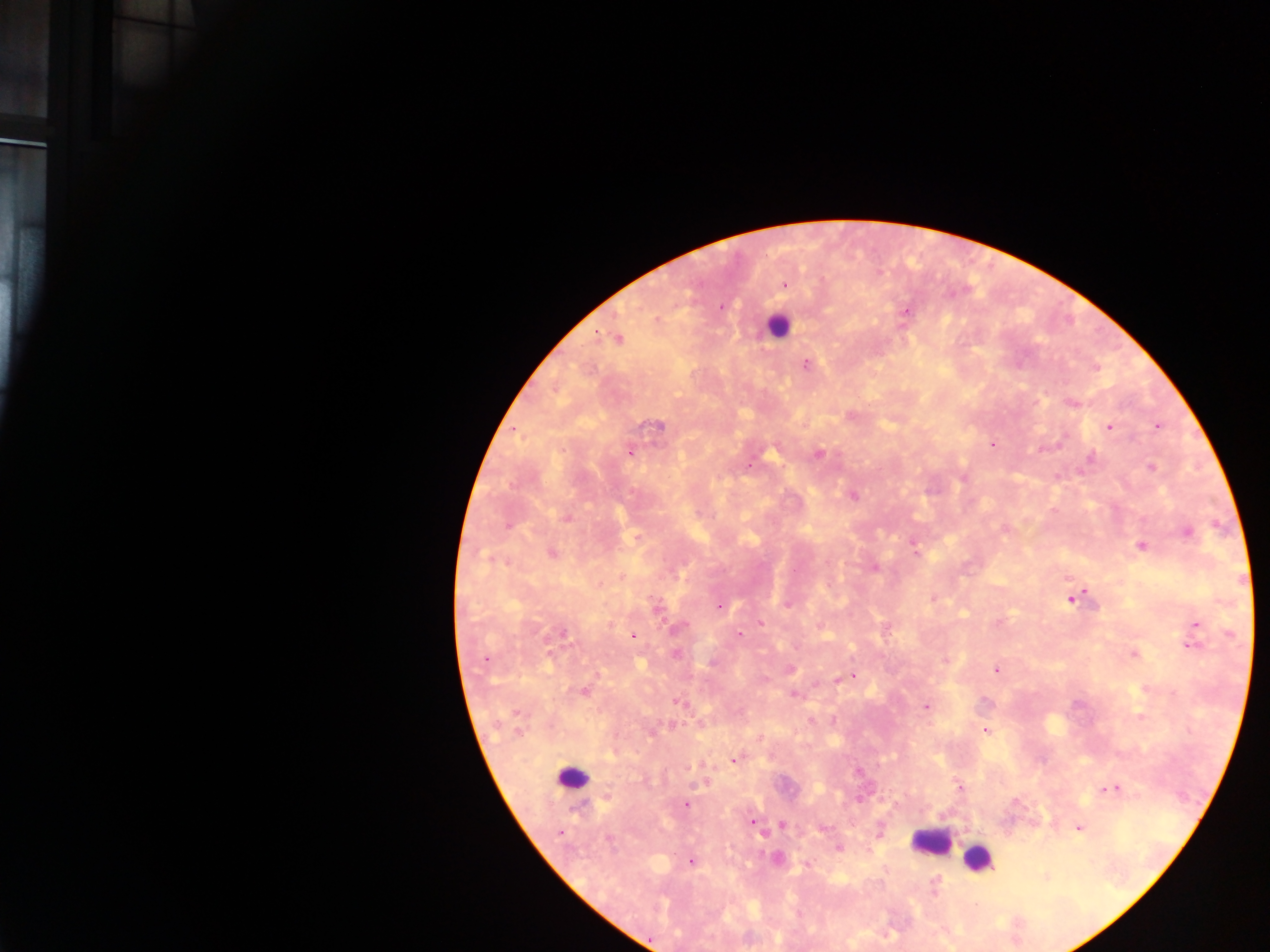 Approximate centers as [x, y] in pixels. Malaria parasite locations: [784, 285], [721, 307], [906, 311], [618, 339], [806, 364], [1073, 403], [657, 425], [1157, 426], [1108, 427], [992, 445], [629, 452], [819, 454], [1091, 457], [749, 466], [1151, 468], [854, 496], [567, 517], [508, 526], [1188, 532], [636, 537], [1141, 546], [916, 552], [552, 554], [875, 568], [1072, 598], [932, 600], [788, 604], [719, 606], [656, 609], [761, 623], [1197, 625], [679, 628], [562, 633], [739, 635], [634, 636], [1192, 645], [675, 654], [1134, 654], [485, 659], [945, 659], [791, 669], [996, 670], [853, 675], [837, 679], [584, 691], [793, 695], [677, 702], [926, 707], [518, 714], [985, 730], [519, 731], [734, 760], [960, 788], [1112, 788], [685, 805], [752, 822], [782, 825], [1078, 827], [824, 828], [560, 833], [610, 840], [838, 849], [691, 863], [807, 864], [934, 884]. Leukocyte locations: [776, 326], [573, 777], [930, 840], [978, 858]. Thick blood smear. Single field of view. Mobile-phone photograph taken through the microscope. Image is 1270×952 pixels. Sample from Ghana.